Point out each leukocyte.
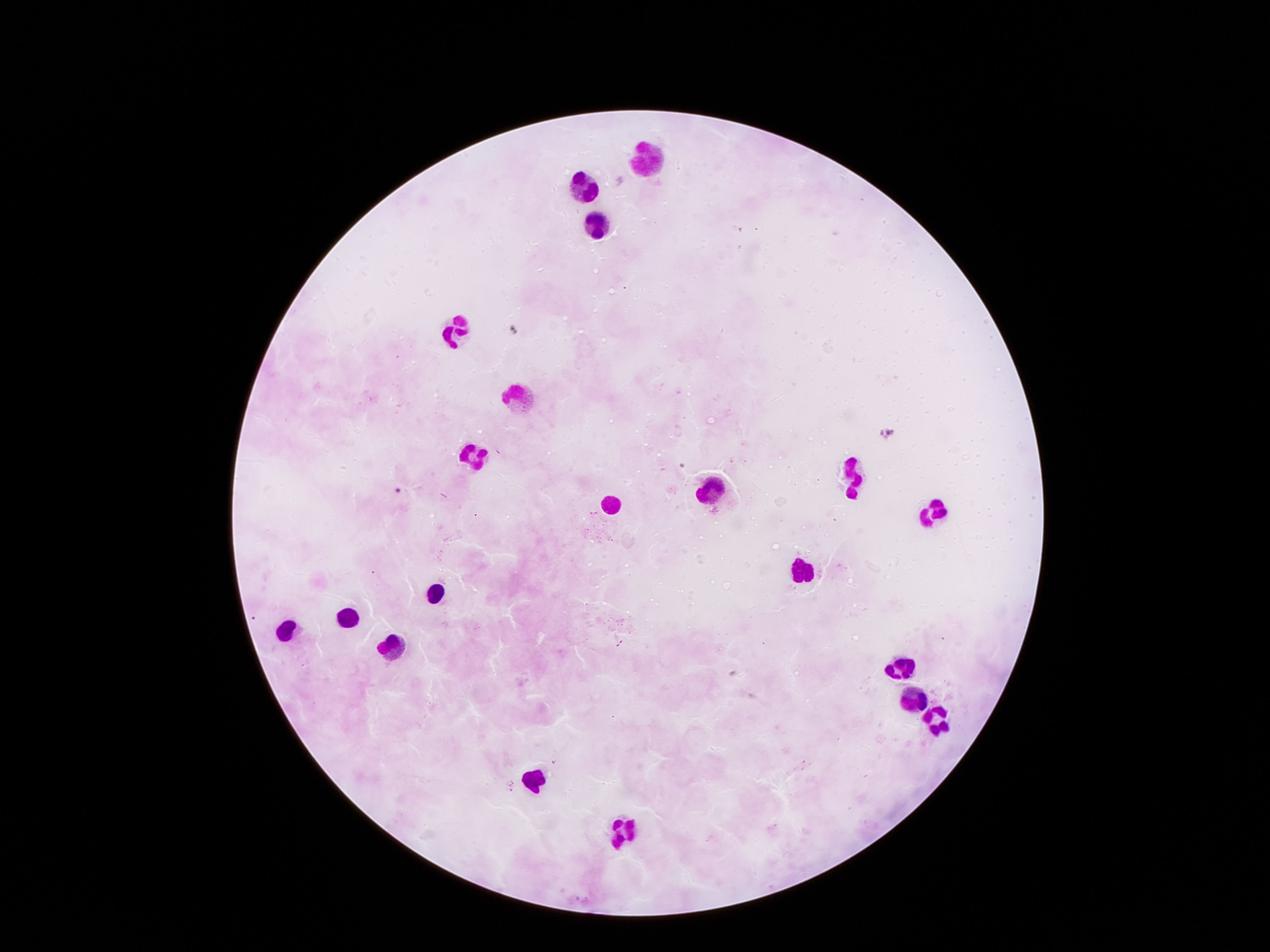
Approximate centers as {x, y} in pixels.
Leukocytes: {646, 157}, {578, 186}, {595, 224}, {455, 330}, {522, 398}, {472, 455}, {848, 481}, {715, 487}, {614, 501}, {932, 513}, {801, 570}, {433, 593}, {348, 617}, {286, 628}, {389, 641}, {898, 670}, {909, 694}, {934, 720}, {534, 779}, {620, 830}.

{
  "magnification": "100x",
  "field_of_view": "single",
  "stain": "Giemsa",
  "patient_malaria_status": "negative",
  "capture": "smartphone camera through the microscope eyepiece",
  "preparation": "thick blood film",
  "image_size": "1270×952 pixels"
}